State the preparation type.
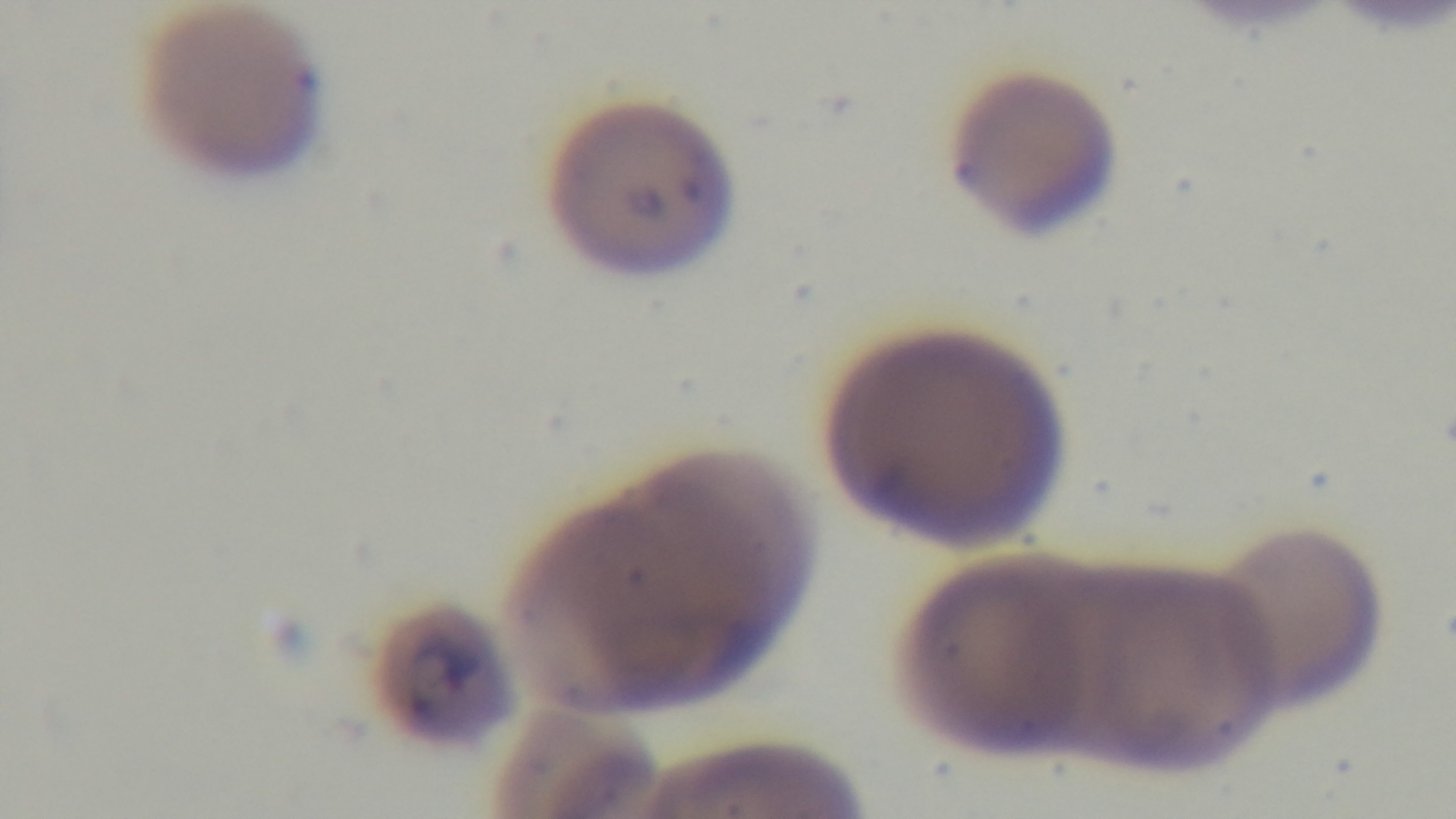
A thin smear.

Oil-immersion objective, 100x. Captured with a mounted 4K digital camera. Malaria status: infected. Photomicrograph. One field from the slide. Giemsa-stained.